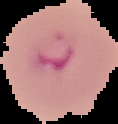
Summary:
  - Result: Plasmodium parasites detected
  - Image size: 118×124 pixels
  - Image type: segmented cell region on a black background
  - Preparation: thin blood film